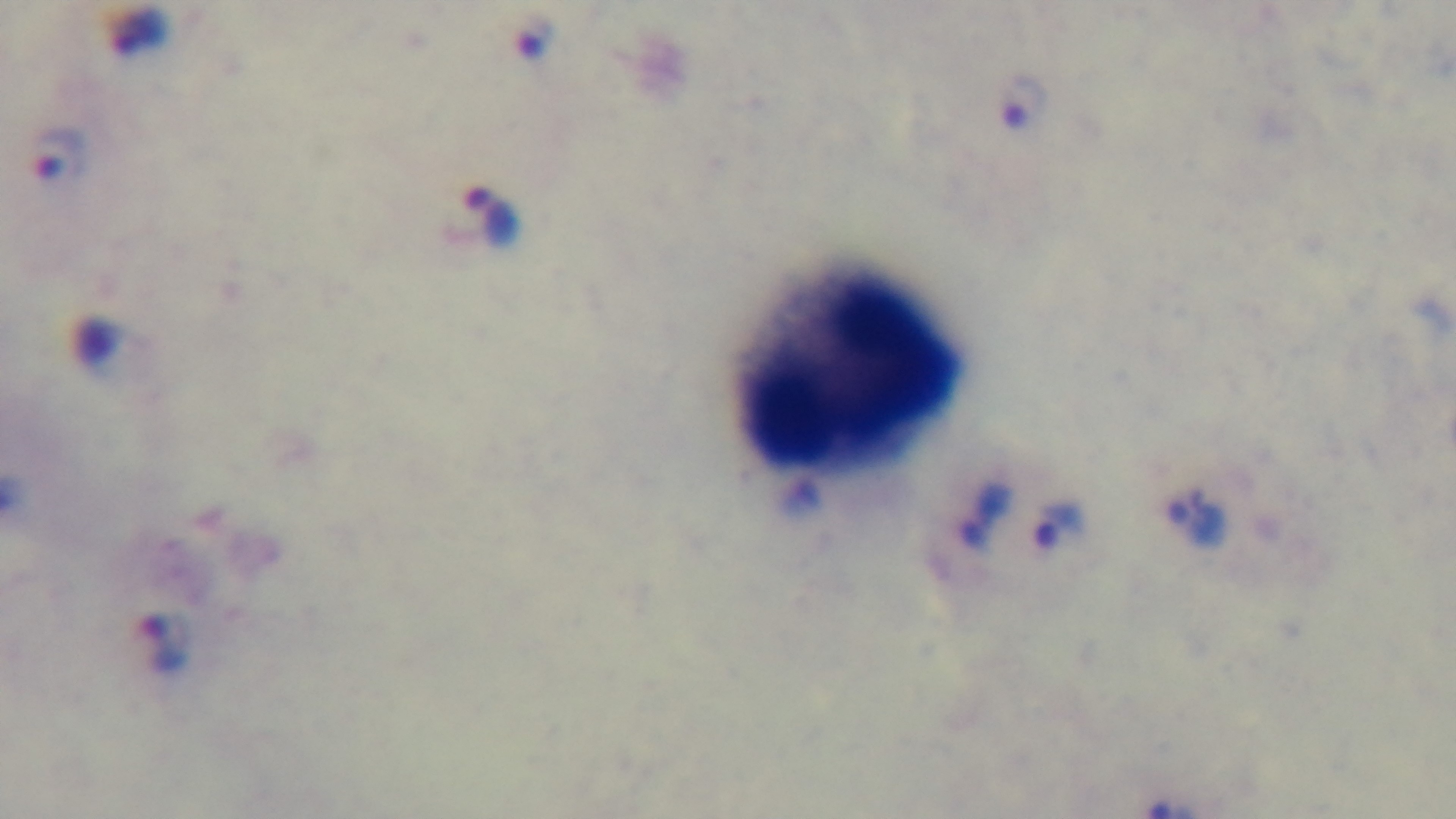
{
  "capture": "mounted 4K digital camera",
  "malaria_status": "positive",
  "field_of_view": "single",
  "stain": "Giemsa",
  "modality": "light microscopy",
  "preparation": "thick smear",
  "objective": "100x oil immersion"
}